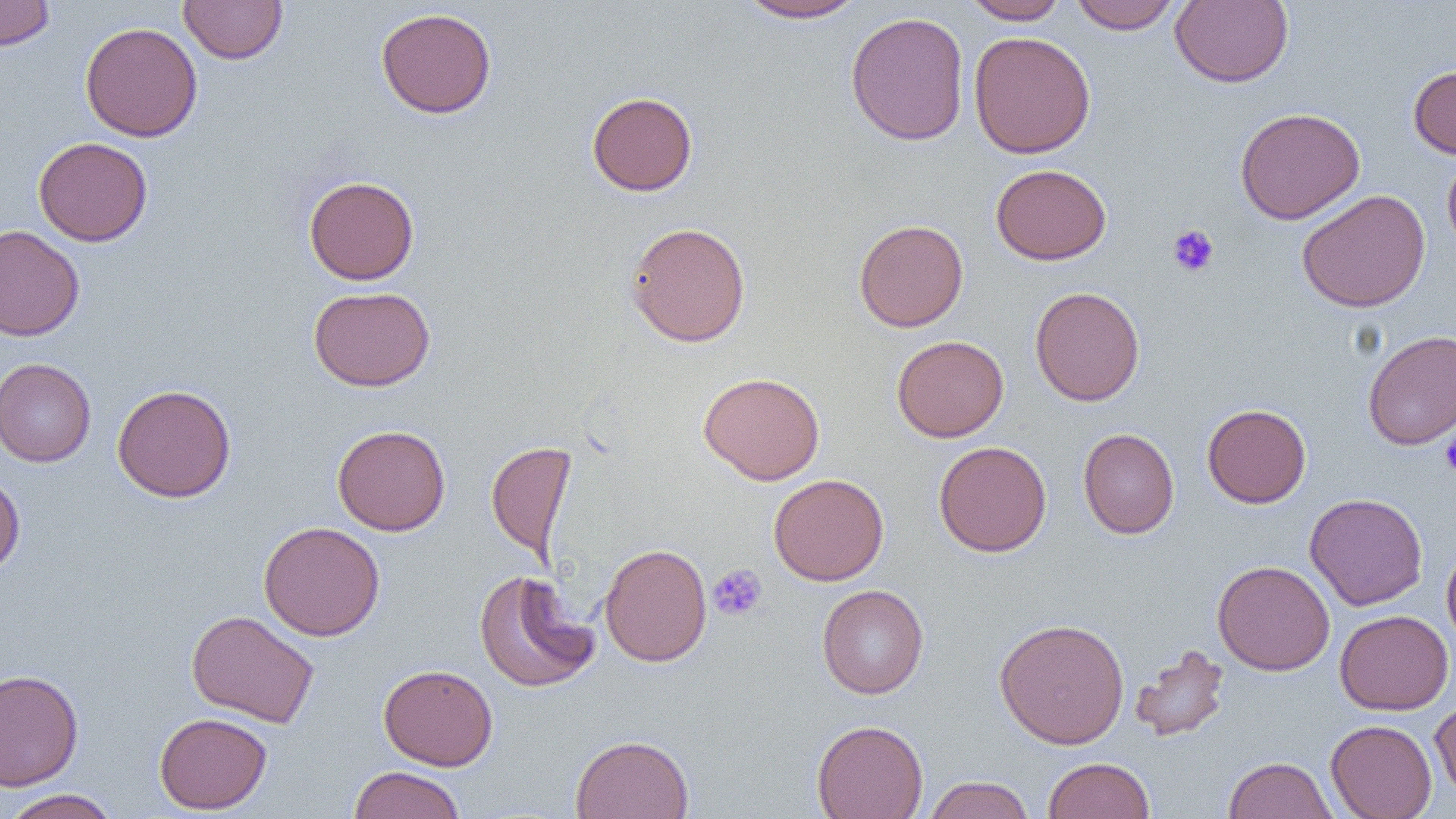
Summary:
  - Coordinate format: approximate bounding boxes as (x1,y1)-(x2,y2) corner pairs in pixels
  - Platelet locations: (1167,224)-(1220,277), (1440,429)-(1456,477), (708,563)-(767,621)
  - Uninfected red blood cell locations: (0,0)-(55,50), (179,0)-(288,64), (736,0)-(869,23), (961,0)-(1069,24), (1068,0)-(1183,34), (1170,0)-(1294,88), (375,7)-(497,119), (846,11)-(970,146), (80,22)-(203,142), (968,31)-(1096,159), (1408,64)-(1456,159), (586,91)-(698,196), (1235,107)-(1365,225), (33,136)-(153,246), (1442,154)-(1456,256), (990,163)-(1112,265), (304,176)-(419,285), (1297,189)-(1431,313), (853,219)-(968,332), (625,221)-(751,347), (0,225)-(85,341), (308,286)-(436,391), (1029,286)-(1145,406), (1363,330)-(1456,449), (892,335)-(1009,442), (0,358)-(97,467), (698,372)-(825,485), (112,384)-(237,503), (1202,403)-(1311,508), (332,424)-(450,535), (1078,428)-(1180,539), (486,441)-(577,563), (933,441)-(1052,557), (768,473)-(889,586), (0,474)-(25,577), (1304,492)-(1428,610), (258,521)-(385,641), (1441,542)-(1456,650), (599,543)-(712,667), (1212,559)-(1335,676), (474,570)-(601,693), (817,584)-(929,699), (1335,609)-(1454,715), (186,610)-(320,728), (994,617)-(1130,749), (1129,643)-(1231,742), (378,664)-(498,770), (0,668)-(85,792), (1430,698)-(1456,802), (154,712)-(272,813), (812,719)-(928,819), (1326,719)-(1437,819), (570,734)-(694,819), (1043,756)-(1155,818), (1223,756)-(1336,818), (347,765)-(466,819), (922,775)-(1036,819), (1,789)-(121,819)
  - Slide-level diagnosis: no evidence of blood parasites
  - Image size: 1456×819 pixels
  - Magnification: 1000x
  - Preparation: thin blood film
  - Modality: light microscopy
  - Field of view: single